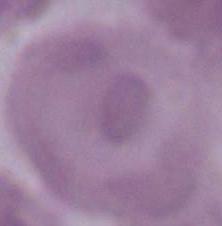

1000x magnification. A red blood cell is shown. Photomicrograph.